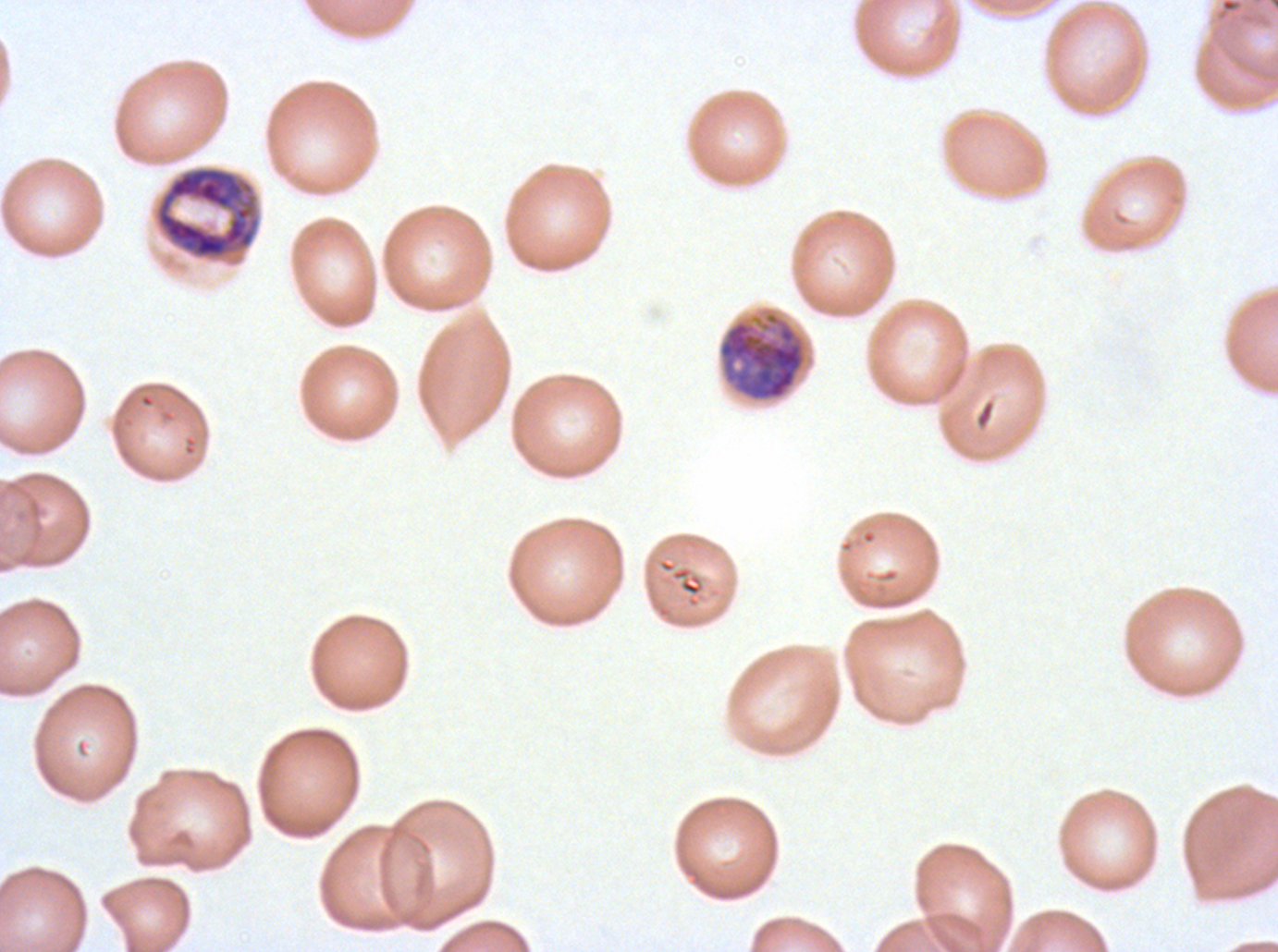

Approximate bounding rectangles given as corner coordinates in pixels from the top-left. Early schizont locations: (x1=154, y1=165, x2=261, y2=261), (x1=717, y1=309, x2=809, y2=403). Thin blood smear. Giemsa-stained preparation. A sub-image separated from a larger composite. Image is 1278×952 pixels. P. falciparum cultured ex vivo for 24 to 48 hours, from a patient in The Gambia.